Describe the morphology of the red blood cells.
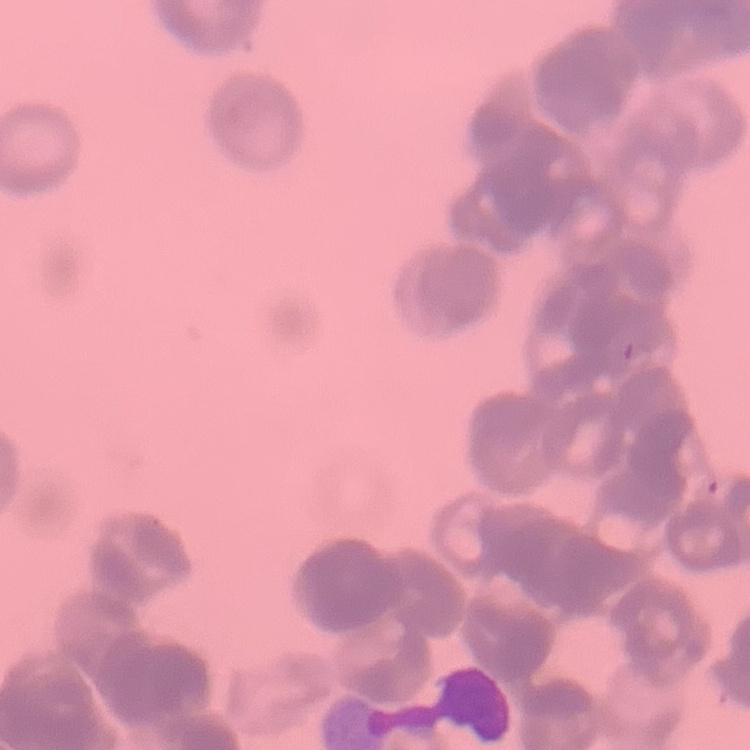

Rouleaux formation.

Summary:
  - Stain: Field's or Giemsa
  - Image type: one tile cut from a larger photomicrograph
  - Preparation: thin blood smear